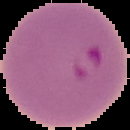

Segmented cell region on a black background. Malaria status: parasitized. Image is 130×130 pixels. From a thin blood smear.